Give the position of every Plasmodium parasite visible.
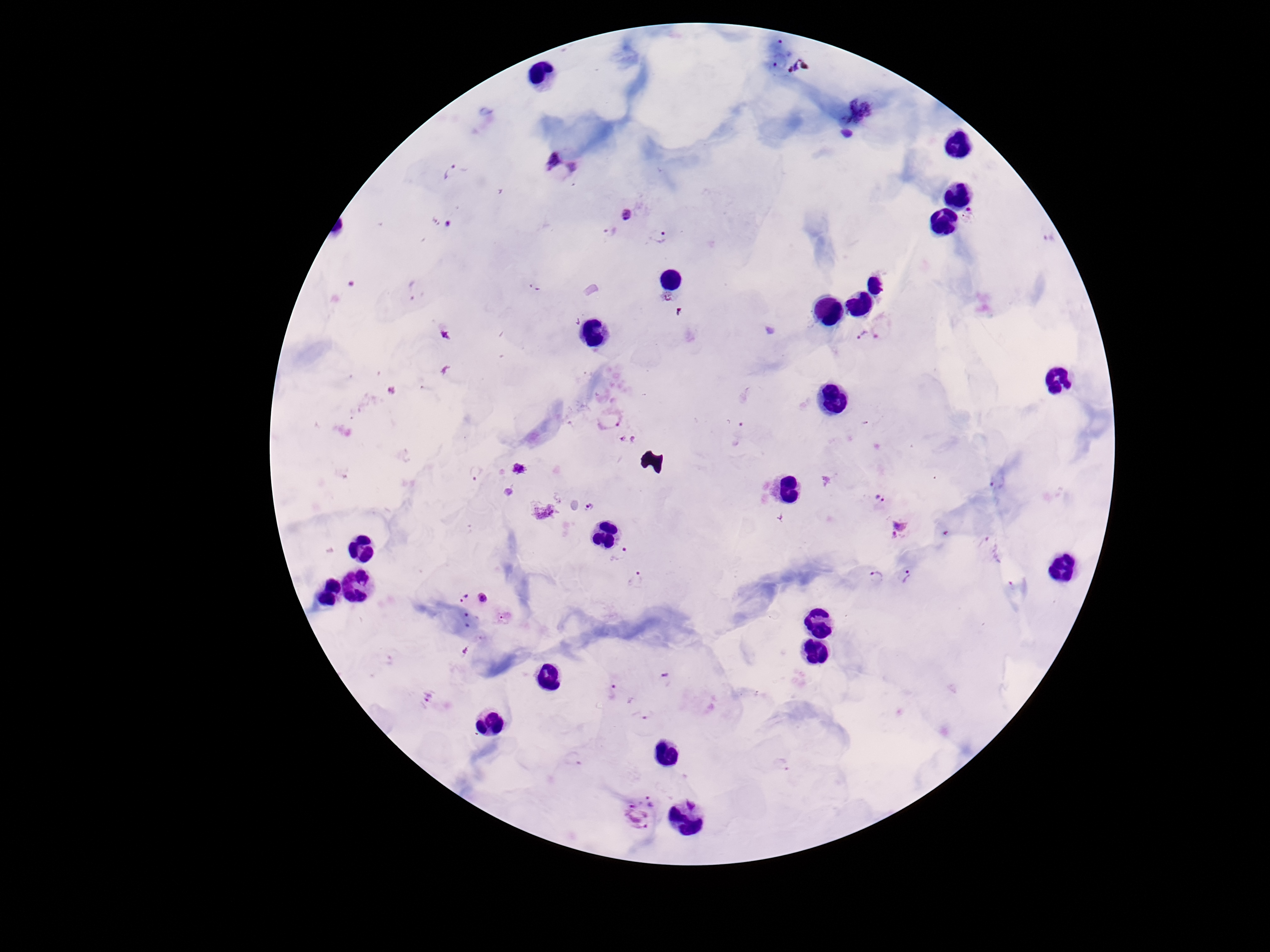

Approximate object centers, in pixels from the top-left corner.
Plasmodium parasites: (x=562, y=166), (x=451, y=173), (x=970, y=214), (x=627, y=217), (x=610, y=231), (x=659, y=235), (x=417, y=291), (x=859, y=336), (x=608, y=420), (x=629, y=441), (x=519, y=469), (x=998, y=482), (x=880, y=499), (x=590, y=508), (x=544, y=512), (x=899, y=529), (x=622, y=556), (x=906, y=576), (x=877, y=577), (x=637, y=580), (x=464, y=598), (x=483, y=598), (x=504, y=618), (x=666, y=679), (x=622, y=693), (x=428, y=695), (x=645, y=716), (x=639, y=813).

{
  "field_of_view": "single",
  "preparation": "thick peripheral-blood smear",
  "stain": "Giemsa",
  "magnification": "100x",
  "image_size": "1270×952 pixels",
  "capture": "smartphone camera through the microscope eyepiece",
  "patient_malaria_status": "positive"
}